Identify the preparation type.
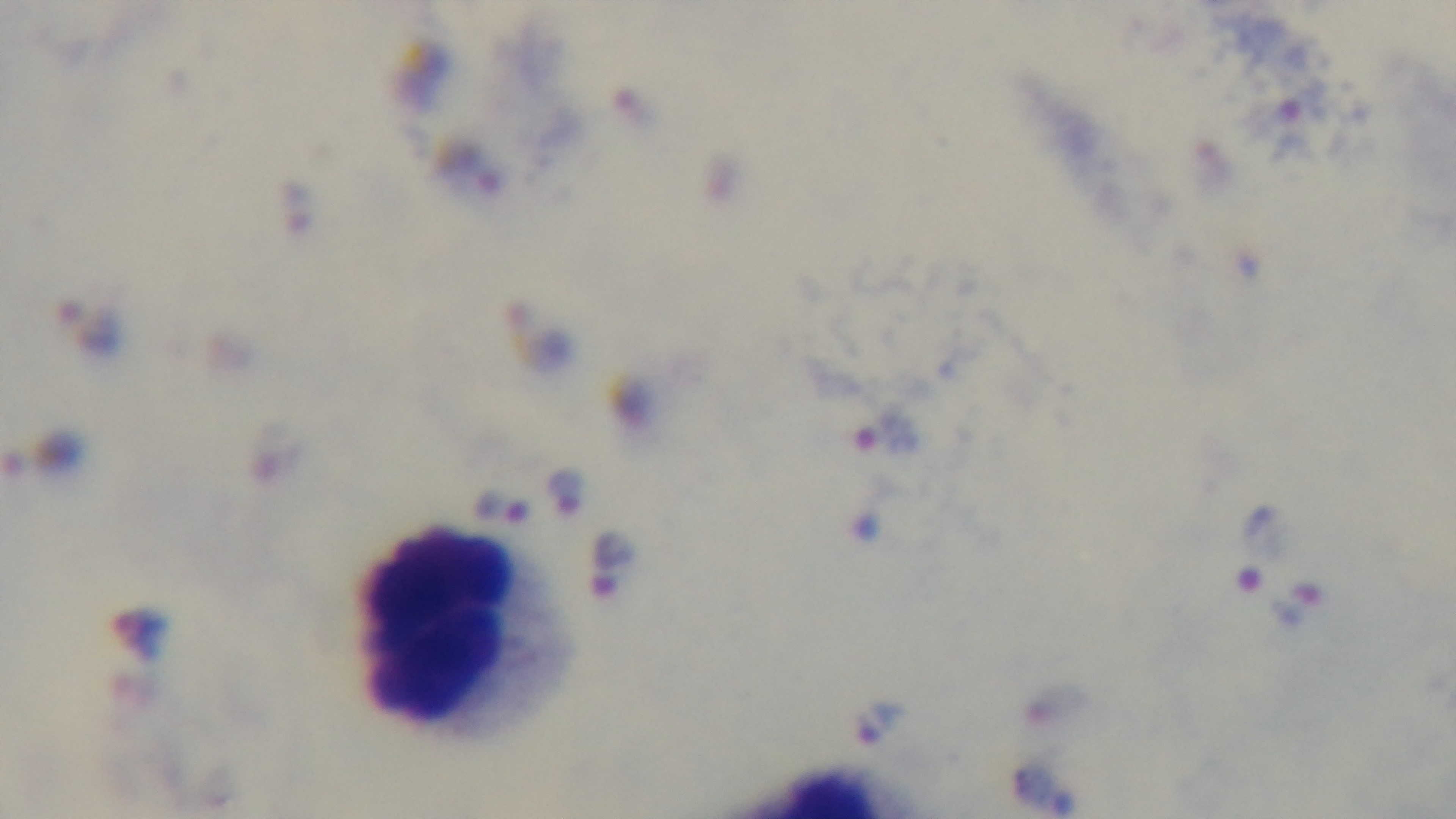
Thick.

Summary:
  - Objective: 100x oil immersion
  - Malaria status: positive
  - Modality: light microscopy
  - Stain: Giemsa
  - Capture: mounted 4K digital camera
  - Field of view: single